Locate every Plasmodium vivax-infected red blood cell.
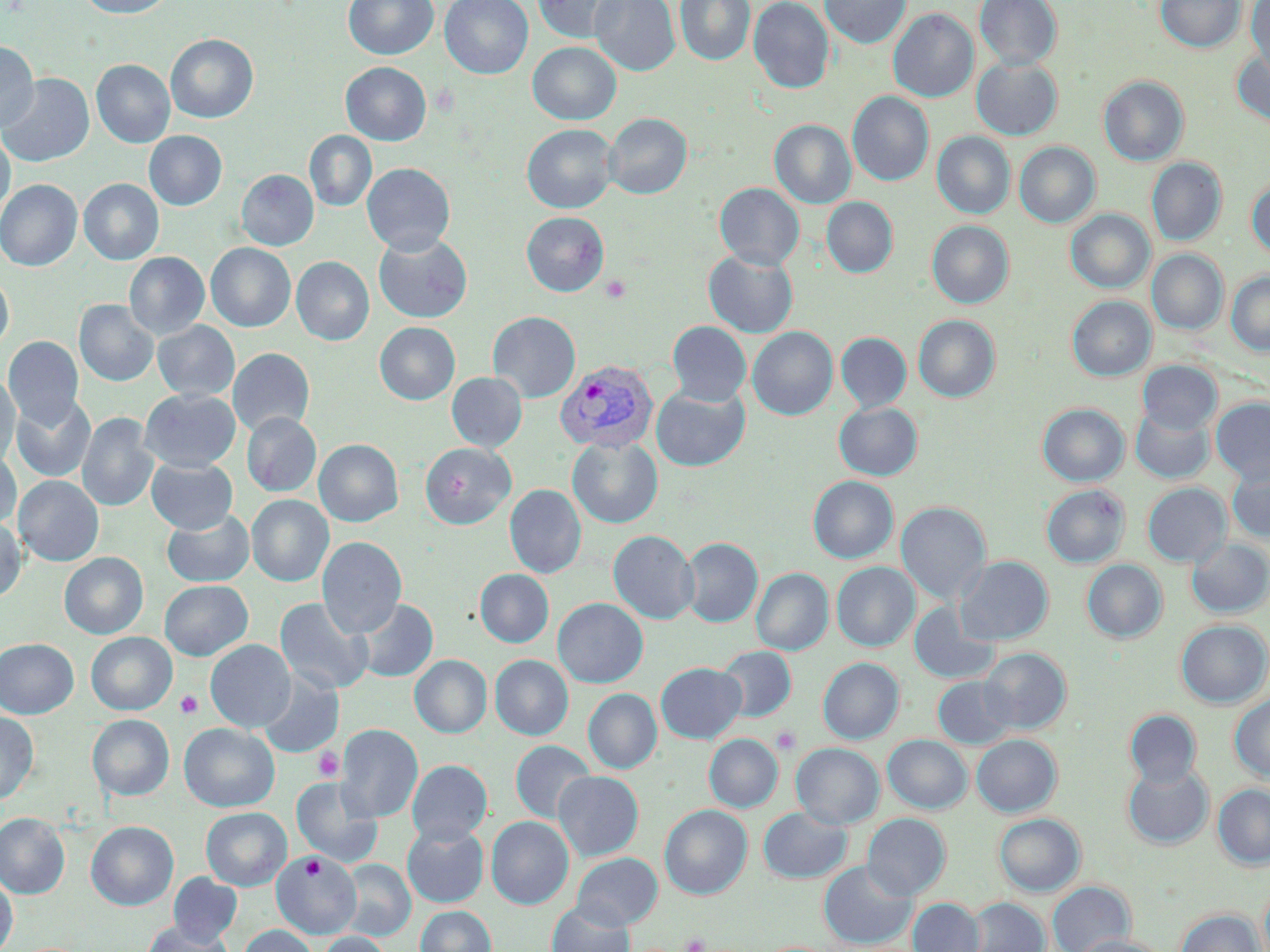
Approximate bounding boxes as (x1,y1)-(x2,y2) corner pairs in pixels.
Plasmodium vivax-infected red blood cells: (555,359)-(659,453).

slide-level diagnosis = Plasmodium vivax
platelet locations = approximate bounding boxes as (x1,y1)-(x2,y2) corner pairs in pixels: (601,274)-(631,303), (175,690)-(203,719), (771,726)-(802,755), (313,748)-(344,781), (301,855)-(325,879), (680,932)-(708,952)
modality = light microscopy
magnification = 1000x
image size = 1270×952 pixels
field of view = one of a larger specimen
preparation = thin blood smear
uninfected red blood cell locations = approximate bounding boxes as (x1,y1)-(x2,y2) corner pairs in pixels: (75,0)-(177,18), (344,0)-(439,60), (440,0)-(533,78), (533,0)-(628,44), (589,0)-(680,76), (675,0)-(755,66), (749,0)-(834,93), (820,0)-(911,48), (974,0)-(1062,70), (1155,0)-(1245,53), (1245,0)-(1270,77), (888,8)-(978,102), (166,34)-(258,123), (0,41)-(39,132), (527,42)-(621,124), (1232,48)-(1270,129), (971,57)-(1063,139), (91,59)-(175,148), (341,62)-(431,145), (0,73)-(94,167), (1098,75)-(1189,166), (847,91)-(934,186), (603,113)-(692,199), (769,120)-(856,208), (522,124)-(618,213), (144,130)-(227,210), (304,130)-(376,211), (932,131)-(1015,218), (0,134)-(15,223), (1014,141)-(1100,227), (1146,157)-(1227,246), (362,163)-(455,254), (236,169)-(319,250), (1247,176)-(1270,258), (79,178)-(164,265), (0,179)-(82,270), (714,183)-(804,270), (822,197)-(898,277), (1065,209)-(1154,293), (521,212)-(609,296), (927,220)-(1014,308), (373,232)-(473,323), (206,243)-(296,332), (1147,249)-(1227,334), (703,251)-(798,338), (124,252)-(209,340), (291,256)-(374,345), (1226,271)-(1270,356), (0,272)-(13,353), (1067,296)-(1156,380), (74,300)-(159,386), (488,311)-(581,403), (913,314)-(1000,402), (153,321)-(240,401), (667,321)-(752,405), (375,322)-(460,405), (748,327)-(838,420), (836,329)-(1001,407), (836,332)-(911,411), (3,336)-(84,429), (227,348)-(315,436), (1138,360)-(1222,434), (447,372)-(527,451), (0,373)-(21,465), (651,385)-(750,471), (139,389)-(241,472), (11,394)-(96,482), (1211,397)-(1270,484), (834,402)-(923,480), (1038,403)-(1129,486), (1130,404)-(1214,483), (77,412)-(159,512), (241,412)-(321,496), (567,435)-(663,528), (314,439)-(403,526), (419,442)-(516,530), (0,451)-(21,528), (146,457)-(238,533), (1227,464)-(1270,542), (13,475)-(104,566), (808,475)-(898,563), (1142,483)-(1231,567), (504,484)-(586,578), (1041,484)-(1130,568), (246,494)-(334,586), (896,502)-(991,603), (162,508)-(255,587), (0,518)-(26,602), (608,530)-(699,623), (317,536)-(407,637), (680,537)-(763,627), (1186,538)-(1270,618), (59,552)-(148,638), (956,555)-(1053,645), (1082,560)-(1167,643), (831,562)-(920,651), (475,568)-(554,647), (751,568)-(833,655), (159,580)-(252,660), (275,597)-(374,695), (552,597)-(648,687), (355,598)-(438,683), (909,601)-(998,684), (1176,620)-(1270,708), (86,632)-(177,715), (0,638)-(79,718), (206,639)-(296,732), (717,646)-(796,721), (979,648)-(1071,733), (409,654)-(492,737), (490,654)-(573,740), (818,657)-(904,743), (656,662)-(746,742), (257,672)-(344,758), (933,676)-(1016,749), (583,688)-(661,773), (1230,692)-(1270,781), (1125,709)-(1201,787), (0,711)-(38,804), (87,714)-(174,800), (179,722)-(279,812), (336,723)-(423,822), (704,734)-(782,812), (972,734)-(1062,817), (883,735)-(972,813), (510,740)-(595,823), (791,743)-(884,828), (407,759)-(492,844), (1123,763)-(1213,849), (553,771)-(643,860), (291,776)-(383,866), (1213,784)-(1270,869), (660,804)-(752,899), (201,807)-(291,890), (758,807)-(851,883), (0,812)-(70,898), (862,813)-(950,900), (994,813)-(1085,896), (486,816)-(573,909), (86,821)-(178,910), (402,824)-(489,907), (272,851)-(361,938), (572,852)-(663,930), (339,859)-(415,941), (819,861)-(915,949), (168,873)-(242,946), (0,874)-(17,952), (1047,881)-(1135,952), (968,897)-(1049,952), (908,898)-(984,952), (547,900)-(634,952), (415,905)-(496,952), (1175,908)-(1265,952), (142,921)-(233,952), (240,925)-(317,952), (317,932)-(393,952), (1072,935)-(1173,952)
stain = May-Grünwald-Giemsa